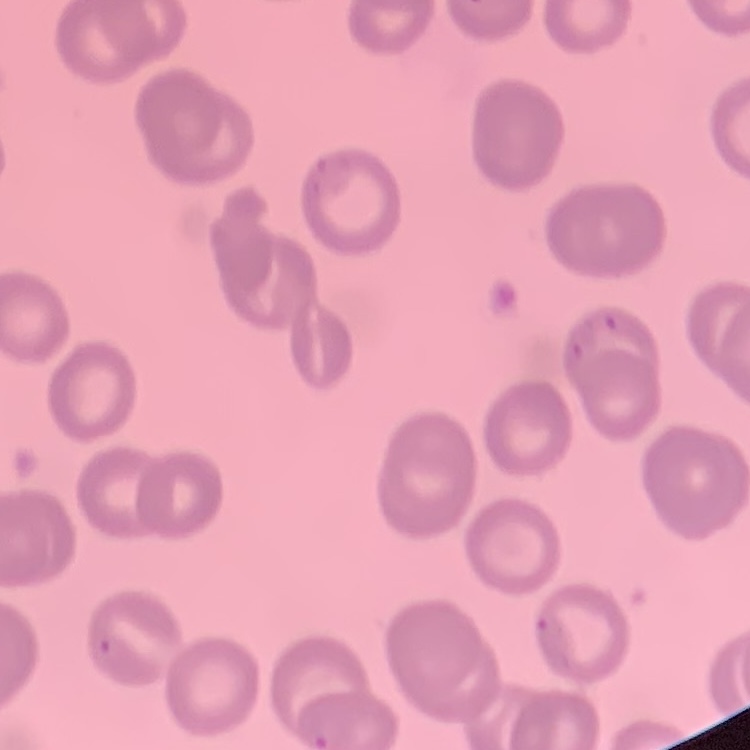 The red blood cells exhibit no rouleaux formation. Square crop of a larger photomicrograph. Stained with either Field's or Giemsa. Thin blood film.